Outline each Trypanosoma brucei.
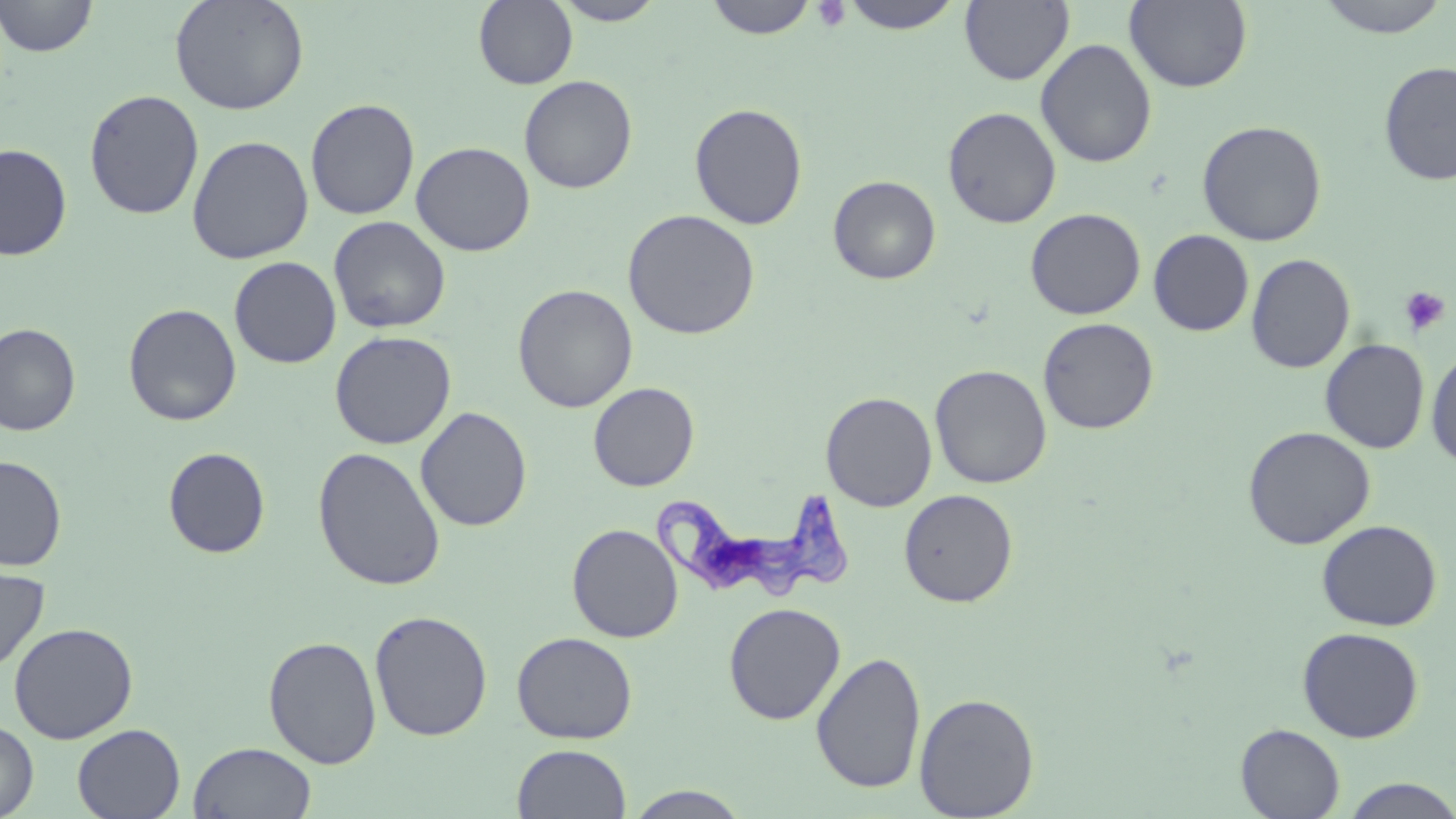

Approximate bounding boxes as [x1, y1, x2, y2] in pixels.
Trypanosoma brucei: [652, 488, 857, 602].

Summary:
  - Platelet locations: [811, 1, 852, 32], [1400, 286, 1450, 335]
  - Uninfected red blood cell locations: [0, 0, 97, 58], [169, 0, 310, 115], [473, 0, 577, 89], [704, 0, 818, 39], [839, 0, 965, 34], [960, 0, 1074, 85], [1125, 0, 1253, 92], [1313, 0, 1453, 38], [552, 1, 665, 25], [1035, 38, 1157, 168], [1379, 61, 1456, 185], [519, 75, 637, 194], [84, 89, 204, 220], [305, 98, 420, 220], [689, 102, 808, 230], [943, 106, 1061, 229], [1197, 119, 1327, 247], [187, 135, 313, 264], [411, 141, 535, 257], [0, 143, 73, 260], [828, 175, 941, 284], [1025, 207, 1145, 320], [622, 209, 761, 340], [328, 215, 451, 334], [1148, 230, 1254, 335], [1246, 253, 1355, 373], [229, 256, 342, 369], [513, 284, 638, 412], [122, 303, 242, 426], [1037, 317, 1159, 434], [0, 323, 81, 436], [329, 330, 456, 450], [1320, 339, 1429, 454], [1425, 347, 1456, 471], [930, 364, 1052, 489], [588, 382, 699, 492], [820, 391, 937, 511], [415, 406, 532, 532], [1242, 426, 1376, 549], [163, 447, 271, 558], [312, 447, 446, 591], [0, 455, 67, 571], [898, 489, 1018, 607], [1316, 520, 1442, 632], [567, 523, 684, 643], [0, 560, 50, 675], [724, 602, 846, 724], [370, 610, 493, 742], [9, 622, 138, 744], [1297, 627, 1424, 742], [512, 631, 638, 744], [263, 636, 382, 769], [811, 651, 927, 794], [914, 693, 1040, 819], [0, 719, 38, 819], [72, 723, 186, 819], [1235, 723, 1345, 818], [188, 741, 317, 819], [512, 744, 631, 819], [1339, 778, 1456, 818], [622, 786, 753, 818]
  - Slide-level diagnosis: Trypanosoma brucei
  - Modality: light microscopy
  - Image size: 1456×819 pixels
  - Field of view: single
  - Magnification: 1000x
  - Preparation: thin blood film
  - Stain: May-Grünwald-Giemsa